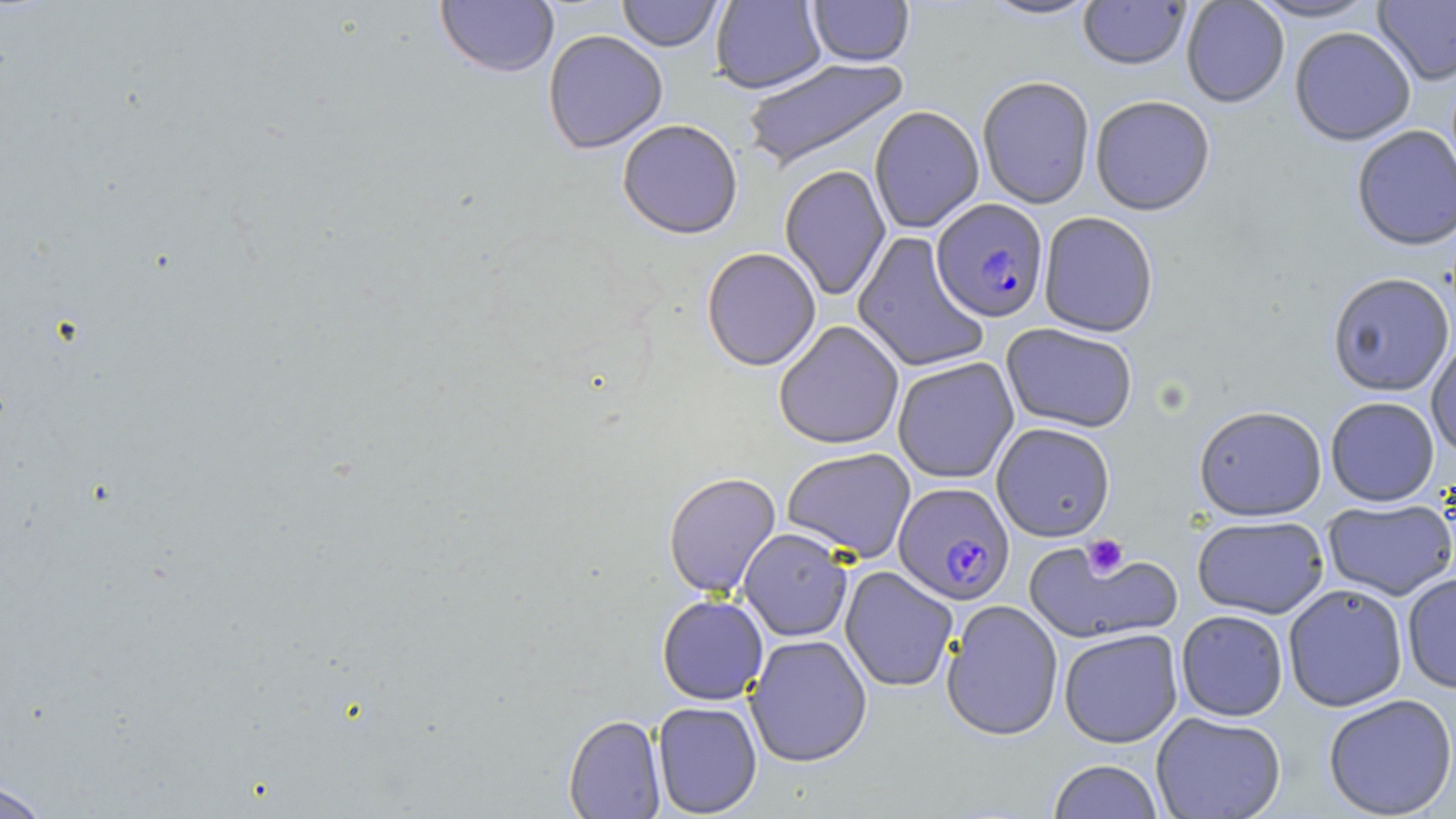

slide_level_diagnosis: Plasmodium falciparum
magnification: 1000x
modality: light microscopy
uninfected_red_blood_cell_locations: 'approximate bounding boxes as (x1, y1, x2, y2) in pixels: (616, 0, 723, 52), (710, 0, 827, 93), (978, 0, 1101, 21), (1078, 0, 1191, 69), (1181, 0, 1289, 108), (1246, 0, 1382, 22), (1373, 0, 1456, 86), (435, 1, 559, 78), (807, 1, 914, 66), (1289, 26, 1416, 145), (542, 29, 668, 154), (741, 56, 910, 172), (977, 75, 1095, 208), (1090, 95, 1216, 215), (869, 105, 984, 233), (617, 119, 744, 238), (1352, 124, 1456, 251), (779, 164, 891, 301), (1038, 211, 1159, 337), (852, 232, 990, 373), (701, 247, 821, 370), (1327, 271, 1455, 396), (773, 320, 905, 450), (1001, 323, 1138, 433), (1426, 333, 1456, 459), (892, 357, 1019, 483), (1325, 396, 1439, 506), (1193, 404, 1327, 521), (991, 422, 1115, 541), (781, 447, 916, 562), (663, 471, 781, 598), (1322, 498, 1456, 601), (1192, 515, 1329, 619), (738, 528, 853, 641), (1023, 537, 1180, 646), (840, 565, 959, 692), (1402, 572, 1456, 693), (1283, 583, 1408, 712), (656, 594, 769, 705), (942, 599, 1063, 741), (1175, 610, 1289, 721), (1059, 628, 1183, 747), (745, 634, 872, 767), (1323, 694, 1456, 818), (652, 701, 762, 817), (1151, 711, 1286, 819), (564, 714, 666, 818), (1047, 759, 1164, 819), (0, 780, 51, 819)'
plasmodium_falciparum_infected_red_blood_cell_locations: 'approximate bounding boxes as (x1, y1, x2, y2) in pixels: (932, 198, 1049, 322), (893, 481, 1015, 605)'
platelet_locations: 'approximate bounding boxes as (x1, y1, x2, y2) in pixels: (1084, 533, 1128, 579)'
image_size: 1456×819 pixels
field_of_view: single
stain: May-Grünwald-Giemsa
preparation: thin blood film